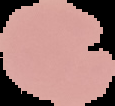

{
  "preparation": "thin blood film",
  "image_type": "segmented cell region with the area outside set to black",
  "image_size": "115×106 pixels",
  "malaria_status": "uninfected"
}